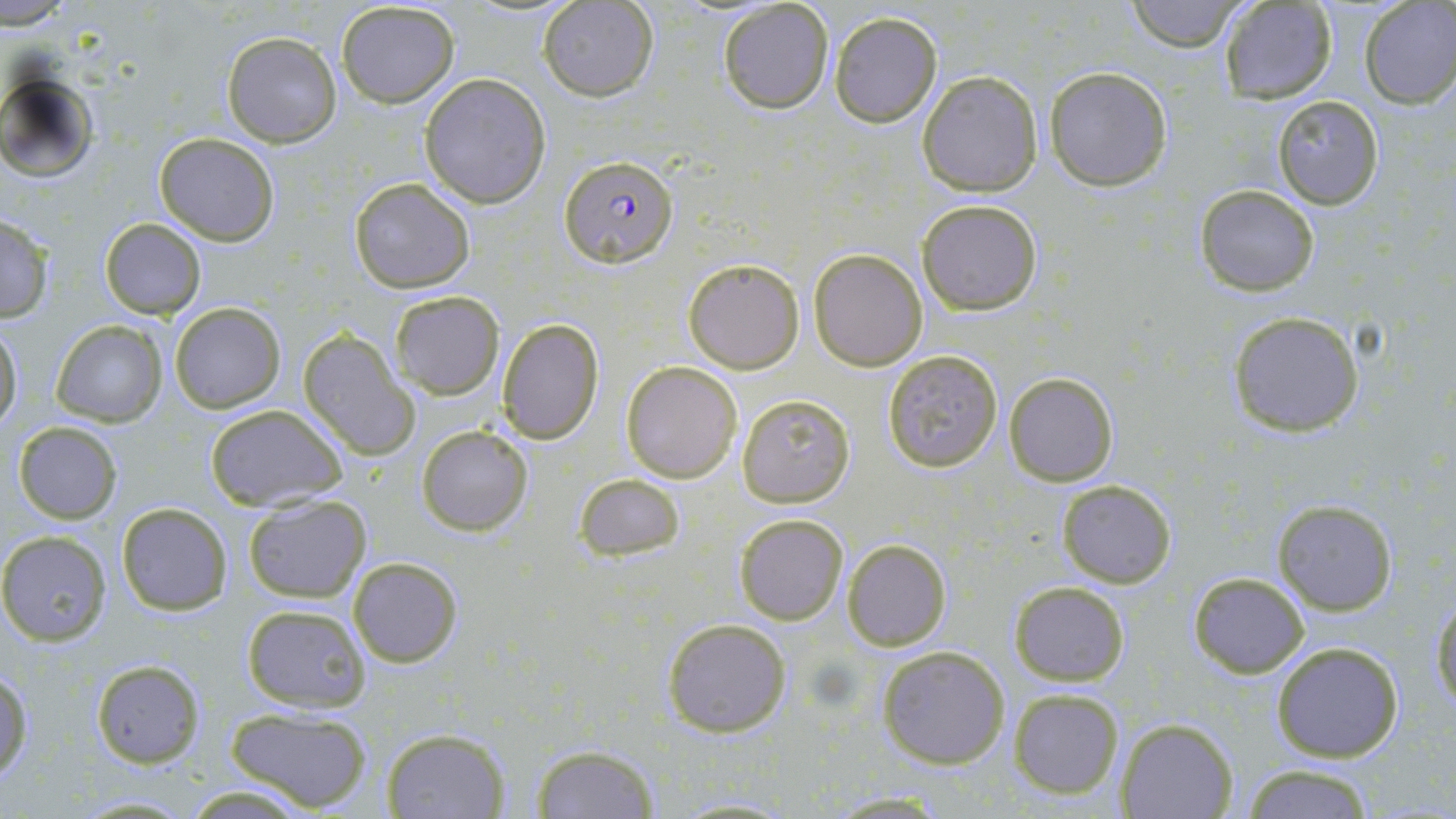
{
  "slide_level_diagnosis": "Plasmodium falciparum",
  "uninfected_red_blood_cell_locations": "approximate bounding boxes as (x1, y1, x2, y2) in pixels: (1123, 0, 1247, 51), (335, 1, 460, 108), (537, 1, 658, 101), (1220, 1, 1338, 104), (1359, 2, 1456, 109), (718, 3, 835, 114), (829, 13, 941, 127), (221, 30, 344, 148), (1044, 66, 1173, 190), (1, 71, 99, 180), (917, 71, 1043, 196), (419, 74, 552, 208), (1271, 96, 1384, 208), (153, 132, 280, 244), (347, 176, 476, 294), (1195, 184, 1320, 296), (916, 199, 1042, 316), (0, 215, 54, 322), (98, 218, 207, 319), (809, 248, 928, 370), (681, 256, 804, 373), (387, 291, 505, 399), (169, 302, 286, 412), (1227, 310, 1365, 437), (496, 317, 606, 444), (49, 319, 169, 427), (0, 324, 22, 431), (296, 328, 420, 461), (881, 350, 1003, 473), (620, 361, 742, 483), (1003, 370, 1119, 486), (737, 395, 854, 508), (203, 404, 349, 513), (12, 421, 122, 524), (415, 425, 535, 536), (574, 473, 685, 561), (1057, 480, 1177, 588), (242, 493, 372, 604), (1271, 499, 1397, 615), (116, 501, 233, 615), (735, 514, 846, 624), (0, 531, 112, 645), (843, 538, 950, 651), (348, 556, 463, 668), (1188, 571, 1308, 677), (1010, 581, 1128, 686), (1430, 596, 1455, 715), (240, 603, 373, 712), (661, 617, 793, 738), (1270, 640, 1404, 763), (877, 644, 1011, 769), (89, 658, 207, 767), (0, 670, 32, 784), (1007, 687, 1124, 799), (223, 705, 376, 812), (1116, 717, 1236, 818), (381, 726, 511, 818), (530, 745, 660, 818), (1242, 764, 1377, 819), (183, 782, 317, 818), (820, 792, 952, 817)",
  "stain": "May-Grünwald-Giemsa",
  "preparation": "thin blood smear",
  "field_of_view": "one of a larger specimen",
  "magnification": "1000x",
  "plasmodium_falciparum_infected_red_blood_cell_locations": "approximate bounding boxes as (x1, y1, x2, y2) in pixels: (560, 155, 678, 270)",
  "image_size": "1456×819 pixels",
  "modality": "optical microscopy"
}